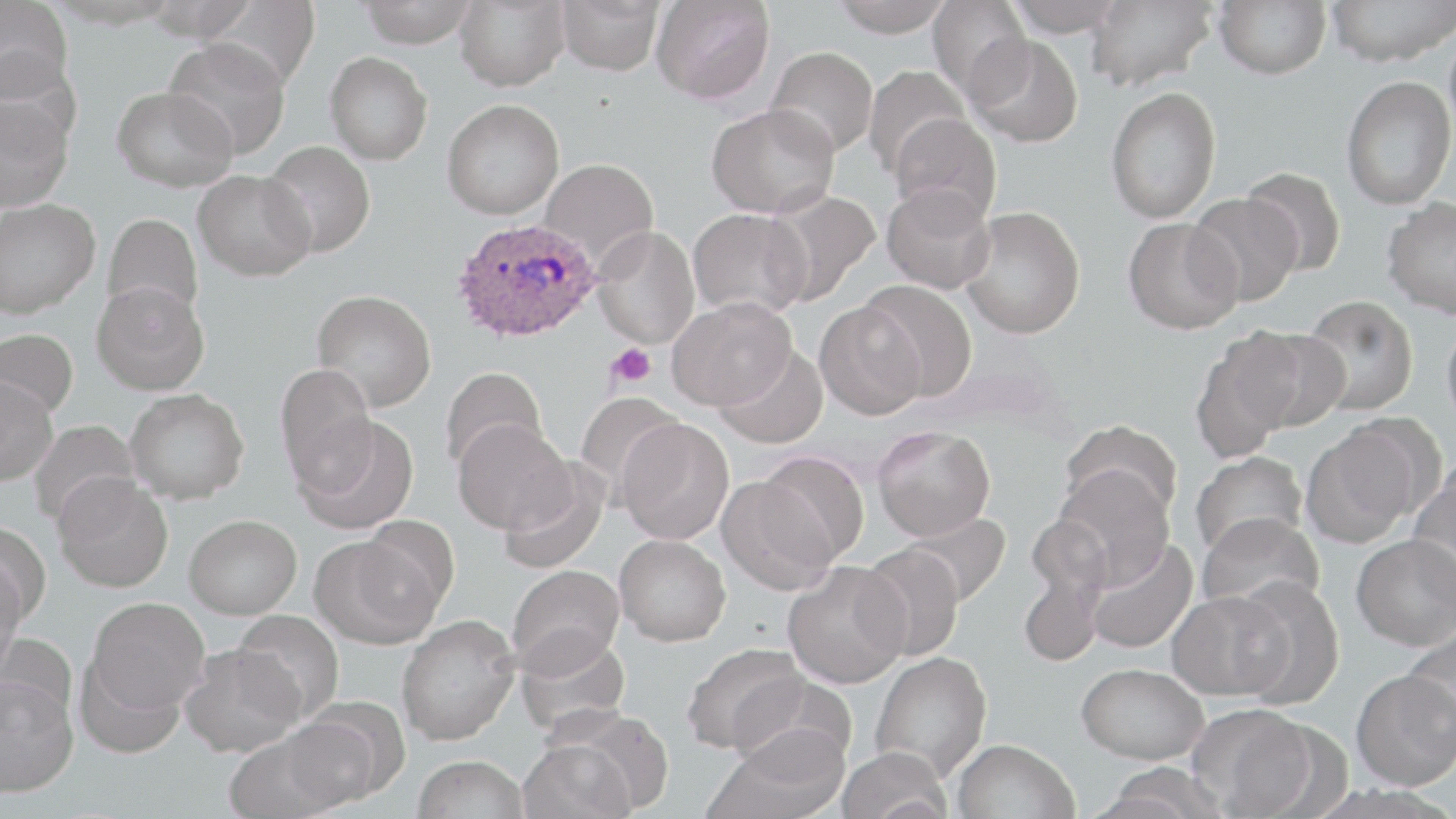

Summary:
  - Coordinate format: approximate bounding boxes as [x1, y1, x2, y2] in pixels
  - Uninfected red blood cell locations: [1, 0, 72, 102], [356, 0, 480, 47], [453, 0, 571, 91], [557, 0, 666, 76], [829, 0, 956, 37], [927, 0, 1032, 99], [1002, 0, 1127, 37], [1086, 0, 1217, 93], [1213, 0, 1331, 79], [1327, 0, 1456, 66], [652, 1, 775, 104], [1444, 19, 1456, 147], [966, 34, 1085, 148], [164, 38, 291, 160], [765, 46, 878, 157], [325, 51, 433, 165], [862, 65, 973, 177], [1341, 76, 1455, 210], [111, 86, 237, 192], [1105, 86, 1221, 224], [0, 93, 74, 212], [442, 99, 564, 220], [706, 103, 840, 219], [888, 112, 1002, 224], [261, 140, 376, 257], [539, 158, 659, 268], [1240, 167, 1347, 276], [193, 169, 315, 281], [881, 182, 997, 295], [762, 189, 881, 305], [1187, 193, 1302, 307], [1382, 197, 1456, 319], [0, 198, 100, 319], [962, 205, 1085, 339], [688, 208, 812, 319], [102, 213, 204, 318], [1123, 218, 1243, 334], [591, 225, 700, 349], [859, 279, 978, 401], [91, 281, 210, 395], [312, 289, 436, 411], [1300, 295, 1419, 416], [667, 297, 795, 410], [814, 303, 925, 421], [1441, 315, 1456, 437], [1234, 326, 1350, 433], [0, 328, 79, 422], [1189, 337, 1295, 463], [713, 346, 829, 449], [274, 364, 377, 490], [440, 366, 548, 473], [0, 377, 58, 485], [125, 389, 249, 503], [574, 393, 686, 500], [1338, 414, 1447, 518], [295, 415, 420, 534], [452, 418, 573, 534], [29, 419, 141, 529], [617, 419, 735, 544], [1060, 420, 1182, 523], [872, 425, 995, 541], [1302, 426, 1420, 548], [1190, 450, 1308, 561], [756, 451, 869, 567], [498, 464, 609, 574], [1051, 466, 1175, 588], [1409, 471, 1456, 594], [53, 473, 173, 592], [717, 476, 839, 595], [1197, 511, 1325, 617], [901, 512, 1010, 608], [184, 514, 302, 618], [0, 522, 52, 630], [614, 533, 731, 646], [310, 534, 442, 649], [1351, 534, 1456, 651], [1085, 538, 1198, 655], [857, 544, 965, 662], [782, 562, 910, 688], [507, 564, 625, 675], [0, 565, 23, 682], [1018, 565, 1105, 668], [1228, 576, 1345, 709], [1167, 589, 1293, 701], [86, 597, 210, 713], [232, 611, 344, 722], [396, 614, 520, 744], [1401, 626, 1456, 748], [514, 629, 631, 738], [180, 643, 305, 756], [681, 643, 808, 756], [870, 651, 993, 781], [75, 654, 186, 758], [1077, 662, 1208, 764], [1351, 669, 1456, 791], [731, 673, 853, 771], [0, 675, 79, 797], [1192, 705, 1322, 818], [277, 709, 394, 813], [707, 725, 849, 819], [223, 732, 347, 819], [517, 738, 636, 819], [952, 739, 1079, 819], [835, 746, 951, 819], [413, 755, 530, 819], [1096, 762, 1232, 818]
  - Plasmodium ovale-infected red blood cell locations: [453, 217, 601, 344]
  - Platelet locations: [606, 343, 656, 386]
  - Slide-level diagnosis: Plasmodium ovale
  - Preparation: thin blood film
  - Magnification: 1000x
  - Stain: May-Grünwald-Giemsa
  - Modality: optical microscopy
  - Image size: 1456×819 pixels
  - Field of view: one of a larger specimen